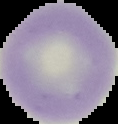
Cell region segmented out of the field of view; the surrounding area is masked to black. Malaria status: uninfected. Image is 118×124 pixels. From a thin blood film.